Describe the morphology of the erythrocytes.
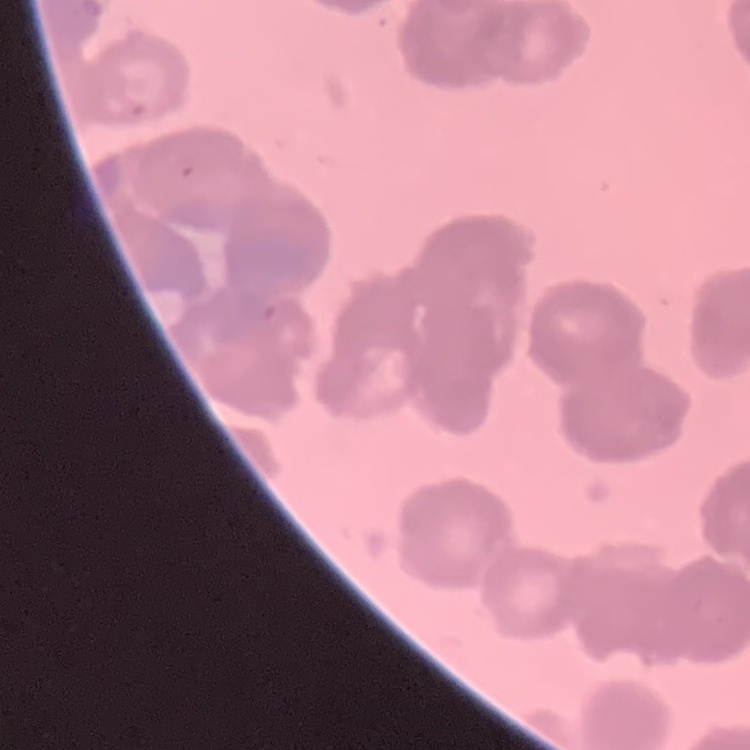
They show rouleaux formation.

stain: Field's or Giemsa
image_type: square crop of a larger photomicrograph
preparation: thin peripheral smear